Give the extent of all Trypanosoma brucei.
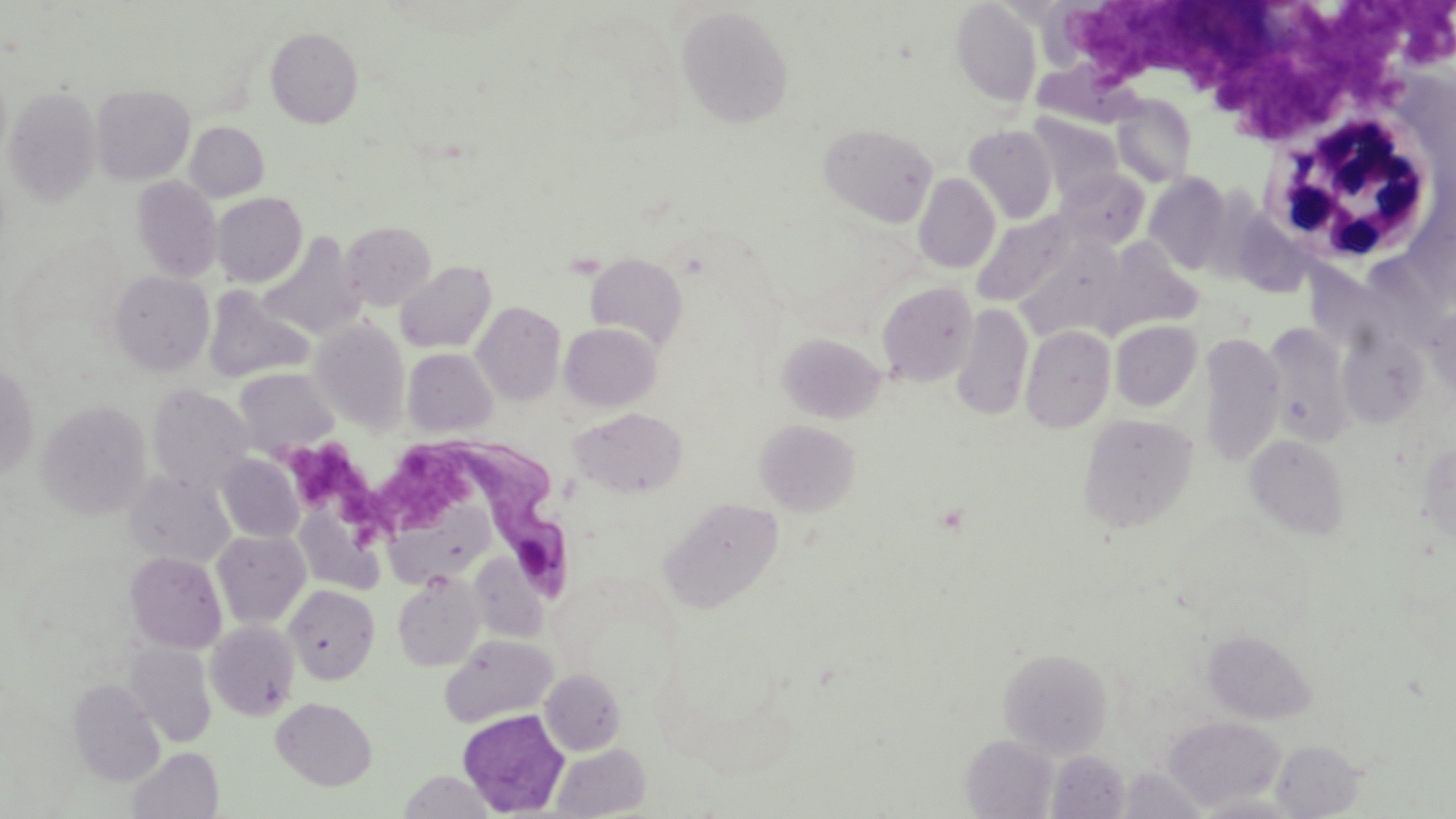

Approximate bounding boxes as (x1, y1, x2, y2) in pixels.
Trypanosoma brucei: (424, 432, 574, 605).

Uninfected red blood cell locations: (951, 1, 1042, 107), (677, 6, 794, 128), (265, 26, 363, 127), (1031, 61, 1136, 127), (92, 84, 195, 184), (5, 88, 101, 206), (1111, 94, 1197, 188), (1027, 113, 1122, 202), (185, 121, 269, 202), (819, 123, 937, 226), (963, 125, 1059, 224), (1055, 169, 1149, 250), (914, 173, 1001, 273), (1144, 173, 1232, 275), (132, 176, 222, 282), (212, 193, 306, 287), (972, 210, 1079, 307), (341, 220, 436, 310), (259, 233, 365, 339), (1096, 238, 1203, 336), (1013, 240, 1124, 340), (584, 253, 689, 350), (395, 260, 496, 353), (109, 272, 214, 376), (875, 281, 978, 387), (203, 287, 313, 383), (472, 301, 566, 405), (952, 303, 1033, 421), (1424, 305, 1455, 401), (311, 318, 410, 432), (1110, 320, 1202, 411), (1262, 321, 1354, 446), (560, 322, 661, 411), (1020, 325, 1116, 433), (777, 332, 887, 423), (1199, 333, 1284, 468), (1340, 333, 1425, 427), (403, 348, 498, 437), (0, 362, 39, 480), (235, 368, 339, 456), (148, 384, 254, 492), (36, 400, 152, 519), (570, 407, 687, 498), (1078, 414, 1197, 533), (754, 419, 860, 516), (1244, 435, 1350, 540), (1415, 440, 1456, 544), (217, 455, 304, 543), (126, 471, 234, 568), (660, 496, 784, 612), (212, 530, 311, 627), (125, 551, 227, 653), (469, 555, 548, 642), (393, 573, 485, 671), (285, 585, 380, 684), (206, 620, 300, 720), (1203, 629, 1315, 723), (440, 635, 557, 728), (126, 642, 217, 747), (998, 648, 1112, 757), (540, 669, 625, 755), (68, 679, 165, 786), (272, 697, 377, 790), (456, 709, 570, 817), (1163, 716, 1285, 811), (961, 734, 1058, 818), (1272, 739, 1367, 817), (550, 743, 651, 818), (129, 747, 223, 819), (1048, 750, 1130, 817), (1120, 767, 1208, 817), (399, 770, 495, 817), (1192, 794, 1306, 818). Platelet locations: (1396, 2, 1455, 70), (1070, 3, 1282, 94), (1303, 7, 1416, 115), (1211, 50, 1350, 131), (279, 442, 365, 507), (382, 448, 469, 530), (336, 472, 387, 540). White blood cell locations: (1262, 112, 1440, 268). Slide-level diagnosis: Trypanosoma brucei. Captured at 1000x magnification. Light microscopy. Image is 1456×819 pixels. Single field of view. May-Grünwald-Giemsa stain. Thin blood smear.